Classify this cell by malaria status.
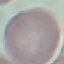
Uninfected.

Summary:
  - Stain: Giemsa
  - Image type: automatically extracted cell patch, resized to 64 × 64 pixels
  - Preparation: thin blood smear
  - Capture: smartphone through the microscope eyepiece